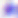
identification: Toxoplasma gondii
magnification: 400x
modality: photomicrograph